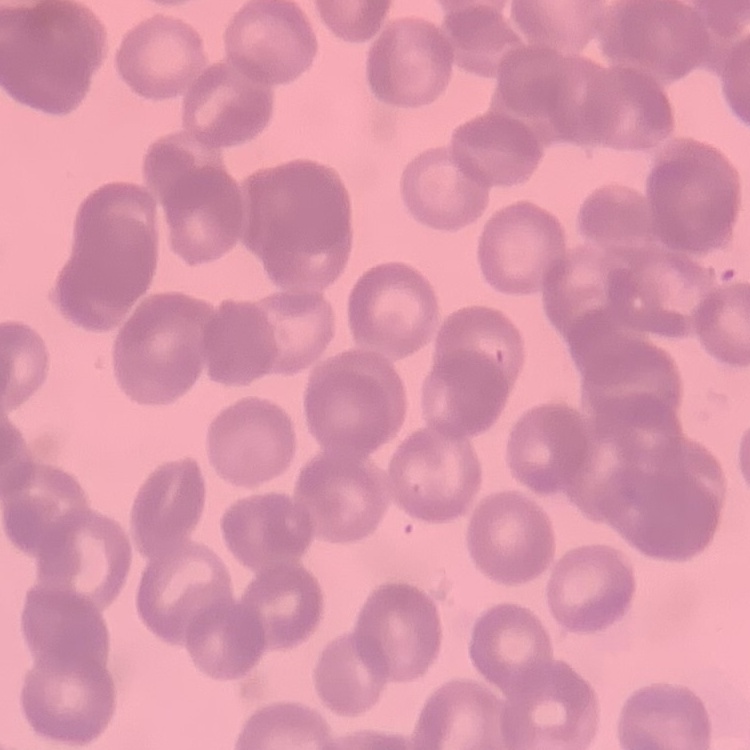

erythrocyte_morphology: rouleaux formation
image_type: one tile cut from a larger photomicrograph
stain: Field's or Giemsa
preparation: thin blood film